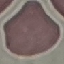
Summary:
  - Result: negative for malaria parasites
  - Capture: smartphone through the microscope eyepiece
  - Preparation: thin blood film
  - Image type: cell patch, automatically extracted from a larger field of view and resized to 64 × 64 pixels
  - Stain: Giemsa